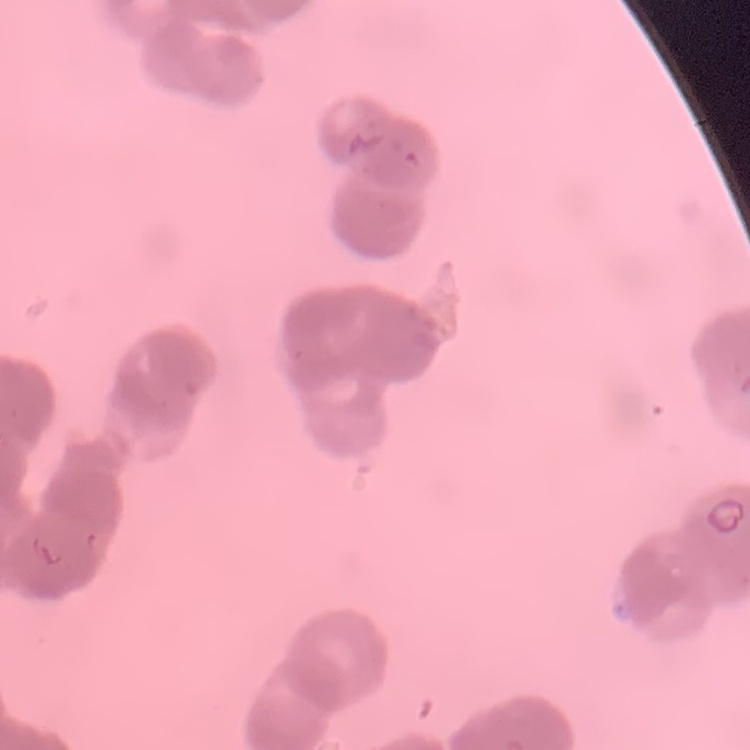
{
  "erythrocyte_morphology": "rouleaux formation",
  "image_type": "square crop of a larger photomicrograph",
  "stain": "Field's or Giemsa",
  "preparation": "thin peripheral smear"
}